Describe the morphology of the erythrocytes.
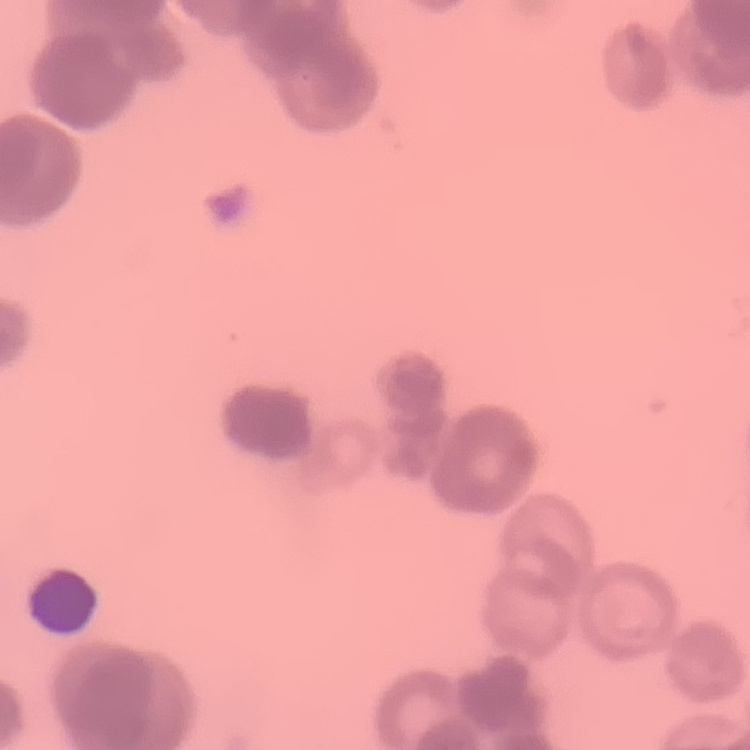

They show rouleaux formation.

Square crop of a larger photomicrograph. Thin peripheral smear. Field's or Giemsa stain.